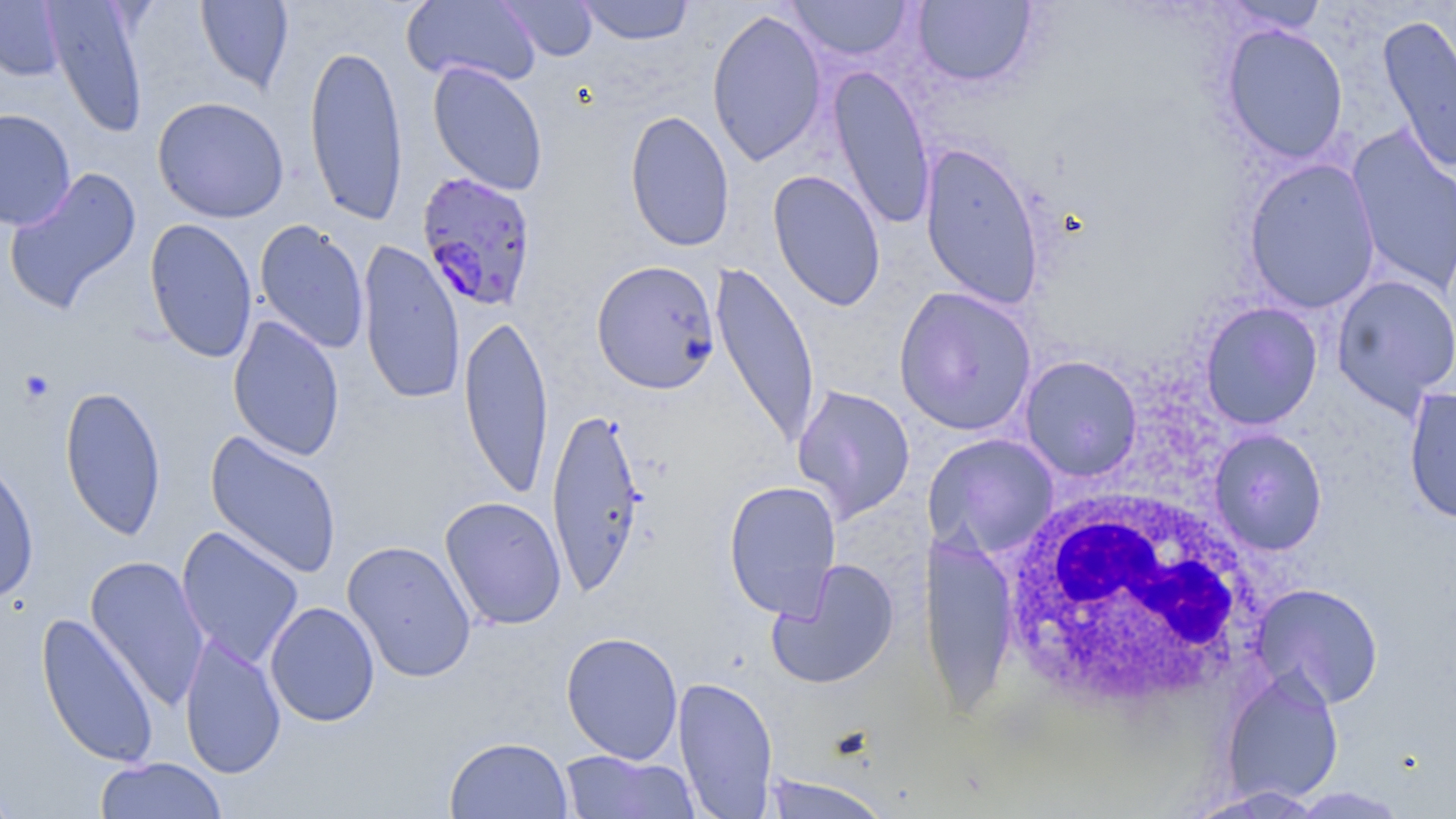

Approximate bounding boxes as [x1, y1, x2, y2] in pixels. White blood cell locations: [999, 486, 1266, 717]. Platelet locations: [17, 370, 55, 405]. Uninfected red blood cell locations: [0, 0, 67, 81], [43, 0, 150, 138], [195, 0, 294, 93], [401, 0, 540, 87], [498, 0, 598, 61], [576, 0, 694, 45], [786, 0, 913, 61], [912, 1, 1038, 88], [1220, 1, 1329, 34], [707, 10, 828, 166], [1377, 12, 1456, 174], [1220, 23, 1349, 165], [304, 42, 408, 226], [427, 61, 549, 197], [827, 64, 936, 231], [152, 96, 289, 223], [0, 108, 76, 230], [625, 109, 735, 252], [1346, 126, 1456, 297], [919, 142, 1044, 310], [1243, 158, 1381, 313], [2, 166, 142, 316], [767, 169, 886, 311], [144, 217, 258, 364], [254, 218, 370, 355], [357, 239, 466, 406], [591, 259, 720, 394], [710, 259, 821, 451], [1331, 273, 1456, 416], [893, 286, 1037, 436], [1199, 301, 1323, 430], [458, 311, 554, 499], [228, 315, 345, 461], [1020, 355, 1143, 482], [791, 383, 915, 523], [59, 385, 167, 541], [1403, 386, 1456, 524], [545, 403, 647, 597], [1208, 428, 1328, 556], [205, 431, 343, 579], [923, 433, 1060, 559], [0, 456, 39, 604], [723, 480, 842, 620], [440, 495, 567, 630], [176, 526, 304, 668], [919, 533, 1018, 717], [341, 539, 477, 683], [85, 555, 210, 710], [767, 559, 899, 689], [1250, 582, 1385, 708], [264, 601, 381, 727], [35, 611, 160, 769], [179, 631, 286, 779], [560, 631, 684, 763], [1221, 668, 1344, 804], [672, 675, 779, 817], [444, 736, 574, 819], [557, 749, 701, 819], [95, 757, 229, 818], [0, 773, 22, 818], [762, 775, 893, 819], [1183, 785, 1328, 818]. Plasmodium falciparum-infected red blood cell locations: [416, 171, 539, 312]. Slide-level diagnosis: Plasmodium falciparum. 1000x magnification. Single field of view. Thin blood smear. Image is 1456×819 pixels. May-Grünwald-Giemsa-stained preparation. Light microscopy.